Describe the morphology of the red blood cells.
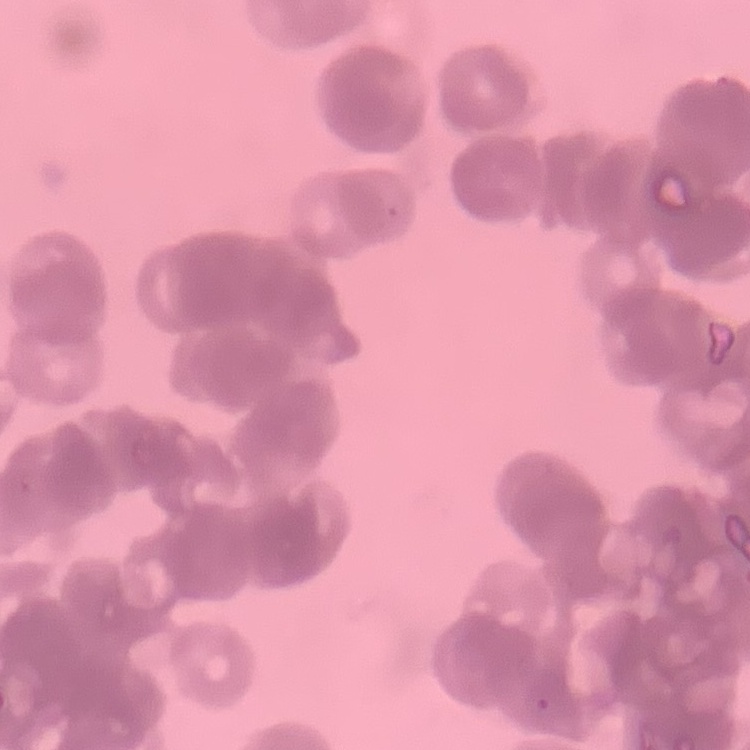
Rouleaux formation.

{
  "image_type": "square crop of a larger photomicrograph",
  "preparation": "thin peripheral smear",
  "stain": "Field's or Giemsa"
}